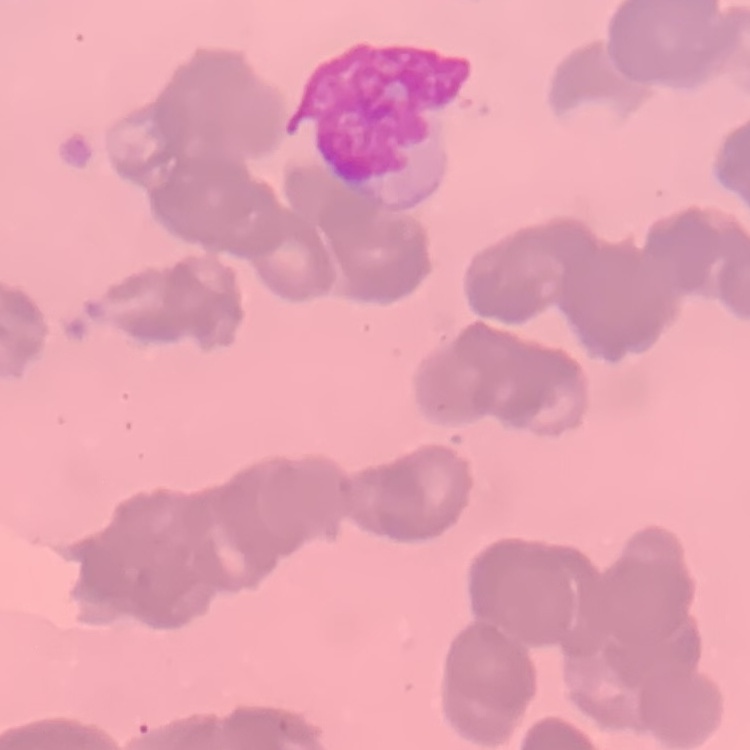
red blood cell morphology = rouleaux formation
preparation = thin blood smear
image type = one tile cut from a larger photomicrograph
stain = Field's or Giemsa